Classify this cell by malaria status.
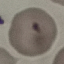
It is uninfected.

image_type: cell patch, automatically extracted from a larger field of view and resized to 64 × 64 pixels
capture: smartphone through the microscope eyepiece
preparation: thin blood smear
stain: Giemsa